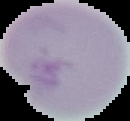

{
  "result": "negative for malaria parasites",
  "preparation": "thin blood smear",
  "image_type": "cell region segmented out of the field of view; surrounding area masked to black",
  "image_size": "130×121 pixels"
}